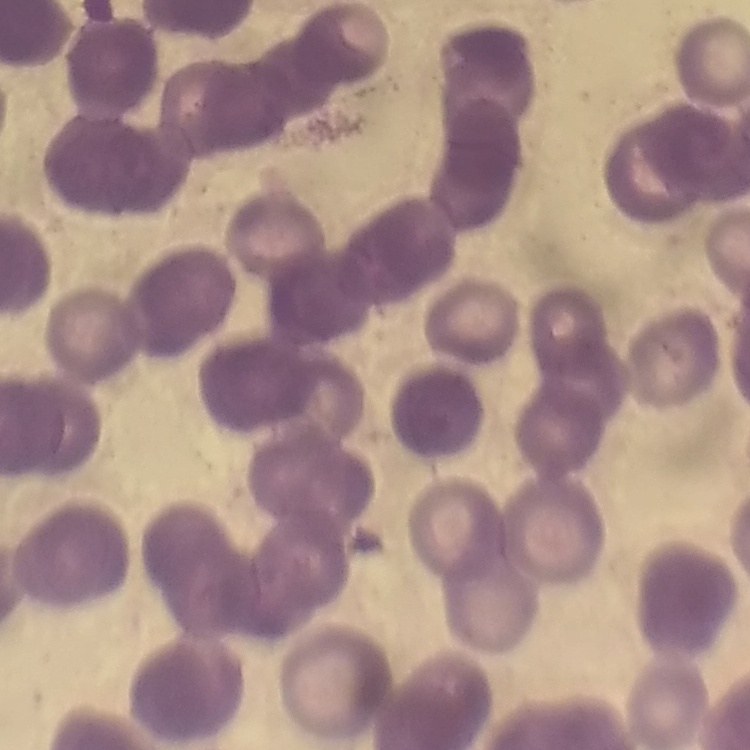

Summary:
  - Red blood cell morphology: rouleaux formation
  - Stain: Field's or Giemsa
  - Image type: one tile cut from a larger photomicrograph
  - Preparation: thin blood smear